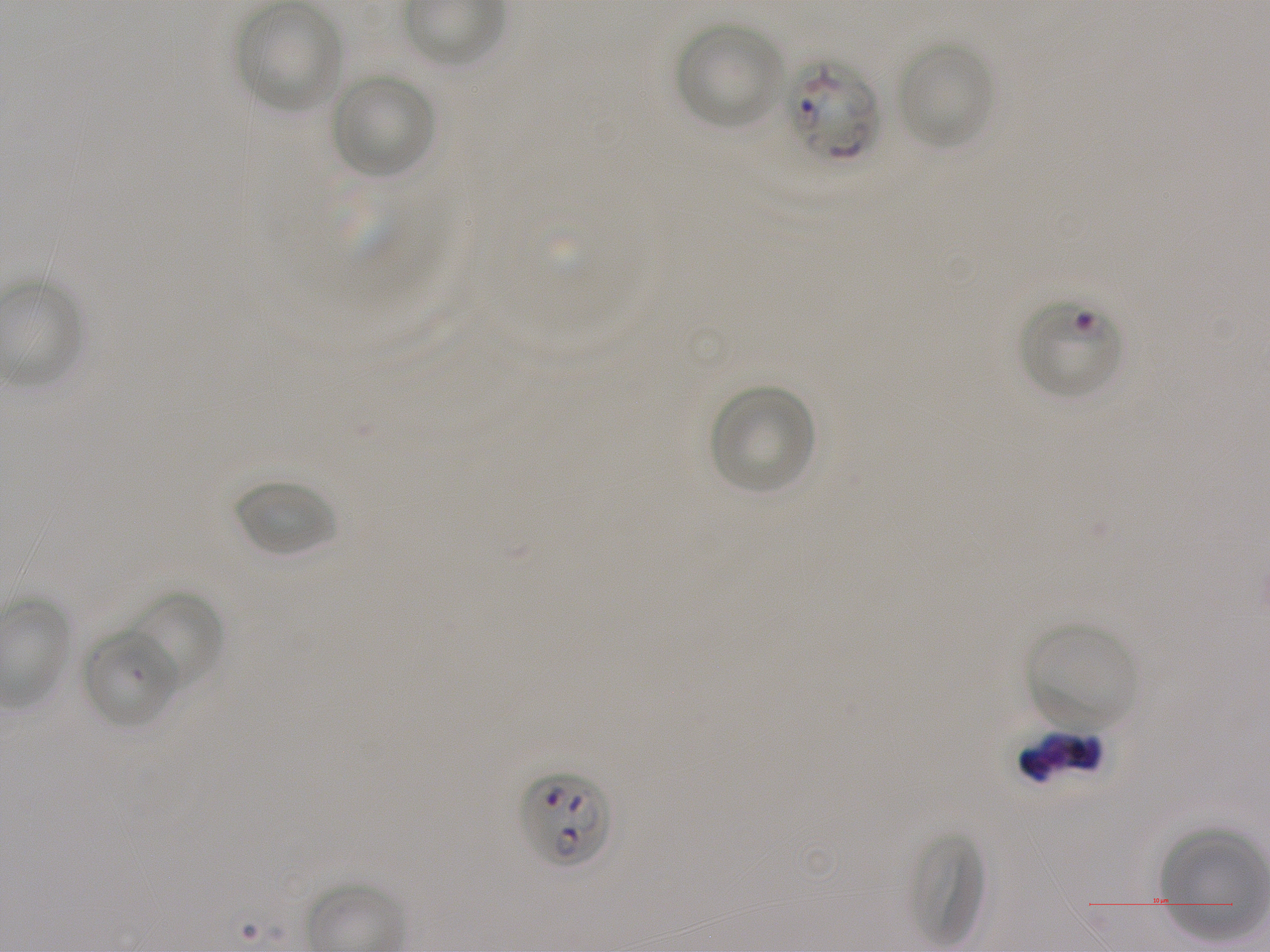

Approximate bounding rectangles given as corner coordinates in pixels from the top-left. Not every red blood cell is marked. A life-cycle stage — or a range of stages, where the recorded stages span more than one — follows each staged infected red blood cell.
Summary:
  - Locations of infected red blood cells: (x1=784, y1=58, x2=878, y2=161); (x1=1018, y1=300, x2=1122, y2=400) ring; (x1=518, y1=770, x2=612, y2=869)
  - Locations of uninfected red blood cells: (x1=237, y1=3, x2=344, y2=112), (x1=675, y1=21, x2=784, y2=129), (x1=897, y1=42, x2=993, y2=150), (x1=331, y1=73, x2=435, y2=179), (x1=708, y1=384, x2=816, y2=495), (x1=234, y1=477, x2=336, y2=557), (x1=127, y1=591, x2=224, y2=692), (x1=1026, y1=622, x2=1138, y2=733), (x1=82, y1=627, x2=181, y2=729), (x1=908, y1=831, x2=986, y2=950), (x1=1161, y1=831, x2=1270, y2=940)
  - Field of view: one from this slide
  - Preparation: thin blood smear
  - Culture: static in-vitro P. falciparum strain NF54
  - Image size: 1270×952 pixels
  - Objective: 100x, oil immersion, numerical aperture 1.25
  - Stain: Giemsa
  - Donor blood group: A+